Report the malaria status of this cell.
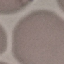

Uninfected.

Giemsa stain. Photographed with a smartphone camera at the microscope eyepiece. Thin smear of blood. Automatically extracted cell patch, resized to 64 × 64 pixels.